Report the malaria status of this cell.
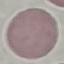
It is uninfected.

Cell patch, automatically extracted from a larger field of view and resized to 64 × 64 pixels. Thin blood film. Acquired by smartphone through the microscope eyepiece. Giemsa-stained preparation.